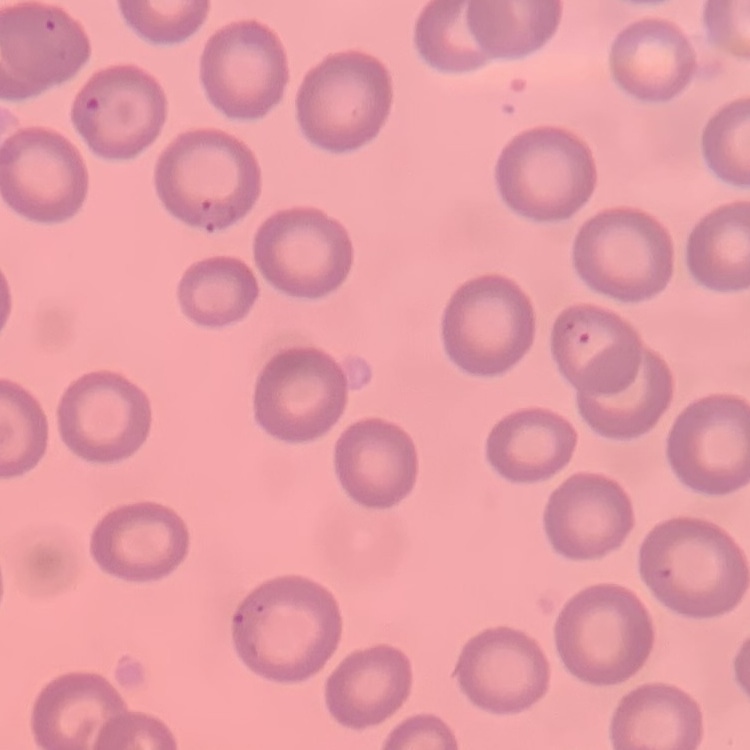

red_blood_cell_morphology: no rouleaux formation
preparation: thin blood smear
stain: Field's or Giemsa
image_type: one tile cut from a larger photomicrograph